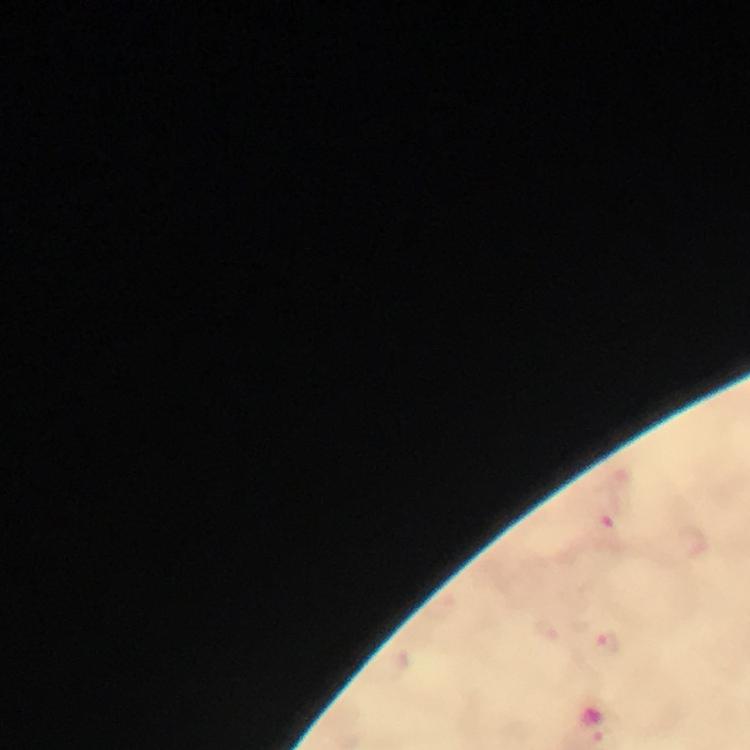
Approximate centers as [x, y] in pixels.
Summary:
  - Malaria parasite locations: [605, 528], [603, 643]
  - Preparation: thick blood smear
  - Cropped from: a single field of view
  - Capture: smartphone camera through the microscope
  - Magnification: 100x
  - Context: from a diagnostic examination for malaria
  - Immersion oil: used
  - Image size: 750×750 pixels
  - Stain: Giemsa